Identify the cell.
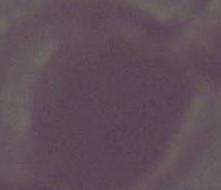
This is an erythrocyte.

Summary:
  - Magnification: 1000x
  - Modality: micrograph